Classify this cell by malaria status.
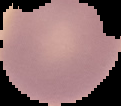

It is uninfected.

Summary:
  - Image type: cell region segmented out of the field of view; surrounding area masked to black
  - Image size: 121×106 pixels
  - Preparation: thin blood smear